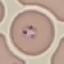
malaria status = parasitized
image type = automatically extracted cell patch, resized to 64 × 64 pixels
preparation = thin smear
stain = Giemsa
capture = smartphone camera at the microscope eyepiece